Give the extent of all uninfected red blood cells.
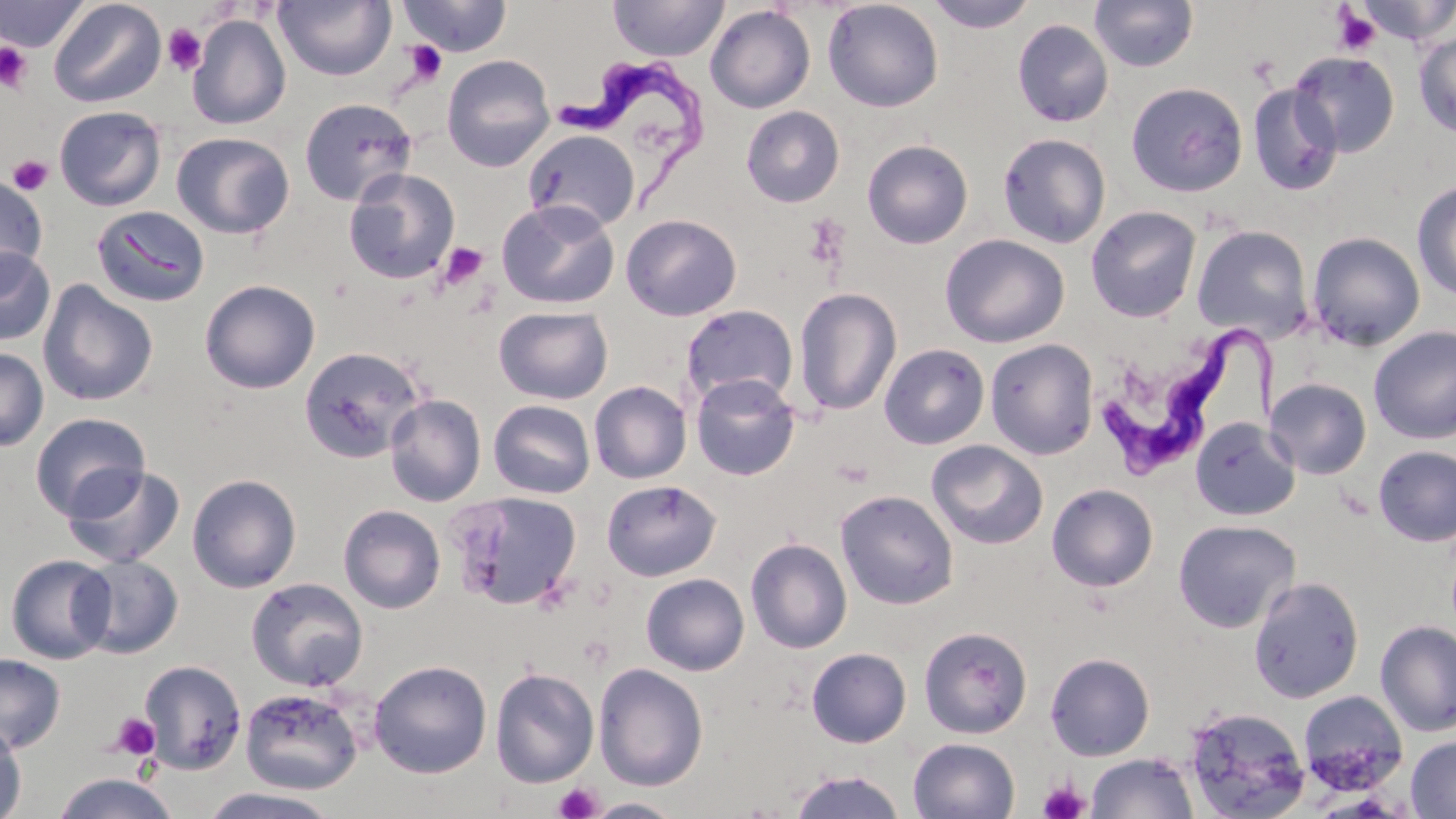

Approximate bounding boxes as (x1,y1)-(x2,y2) corner pairs in pixels.
Uninfected red blood cells: (0,0)-(90,53), (48,0)-(166,108), (274,0)-(395,81), (397,0)-(512,57), (608,0)-(729,62), (822,0)-(944,112), (924,0)-(1038,33), (1089,0)-(1199,72), (1352,0)-(1456,45), (705,5)-(816,113), (186,13)-(291,129), (1012,18)-(1113,128), (1413,31)-(1456,139), (1289,51)-(1400,158), (442,54)-(555,173), (1125,81)-(1248,197), (1247,83)-(1343,196), (299,97)-(417,206), (54,105)-(167,211), (741,106)-(845,207), (522,129)-(639,232), (171,131)-(294,239), (997,133)-(1111,248), (862,139)-(973,249), (343,168)-(461,285), (0,173)-(48,284), (1412,181)-(1456,302), (496,200)-(620,309), (1085,205)-(1202,322), (91,206)-(211,308), (620,213)-(742,321), (1191,224)-(1314,343), (1306,231)-(1426,352), (939,233)-(1070,348), (0,246)-(55,346), (200,279)-(320,394), (37,280)-(159,407), (793,288)-(902,416), (680,304)-(799,409), (494,306)-(613,404), (1369,326)-(1456,444), (985,338)-(1099,460), (880,343)-(989,449), (298,346)-(426,463), (0,347)-(48,452), (690,374)-(800,480), (1265,377)-(1372,479), (589,381)-(692,484), (385,395)-(486,506), (488,399)-(596,499), (30,412)-(150,521), (1189,416)-(1301,521), (926,439)-(1048,549), (1373,445)-(1456,547), (62,464)-(185,569), (187,474)-(302,593), (601,479)-(721,581), (1046,484)-(1159,591), (835,490)-(959,609), (448,491)-(582,609), (338,504)-(446,614), (1172,519)-(1301,633), (746,538)-(852,654), (5,554)-(116,664), (73,555)-(184,659), (641,573)-(749,676), (1248,576)-(1364,703), (246,577)-(368,691), (1374,619)-(1456,737), (918,626)-(1033,739), (806,642)-(1033,744), (806,647)-(912,748), (1045,652)-(1155,761), (0,654)-(66,753), (140,660)-(247,774), (369,660)-(492,778), (593,662)-(709,791), (489,668)-(599,788), (240,687)-(363,795), (1297,689)-(1409,795), (1182,705)-(1311,819), (0,721)-(27,819), (1406,735)-(1456,818), (908,737)-(1020,819), (1086,752)-(1199,818), (787,770)-(907,818), (51,771)-(178,819), (194,787)-(344,819), (585,798)-(685,818).

Trypanosoma brucei locations: (562,59)-(720,211), (1099,325)-(1284,470). Platelet locations: (1330,5)-(1382,56), (162,23)-(207,76), (402,40)-(448,86), (0,42)-(33,93), (7,154)-(54,196), (437,242)-(489,291), (109,713)-(162,761), (1038,778)-(1090,819), (554,783)-(603,819). Slide-level diagnosis: Trypanosoma brucei. Optical microscopy. Thin blood film. 1000x magnification. Single field of view. May-Grünwald-Giemsa stain. Image is 1456×819 pixels.